Give the position of every malaria parasite.
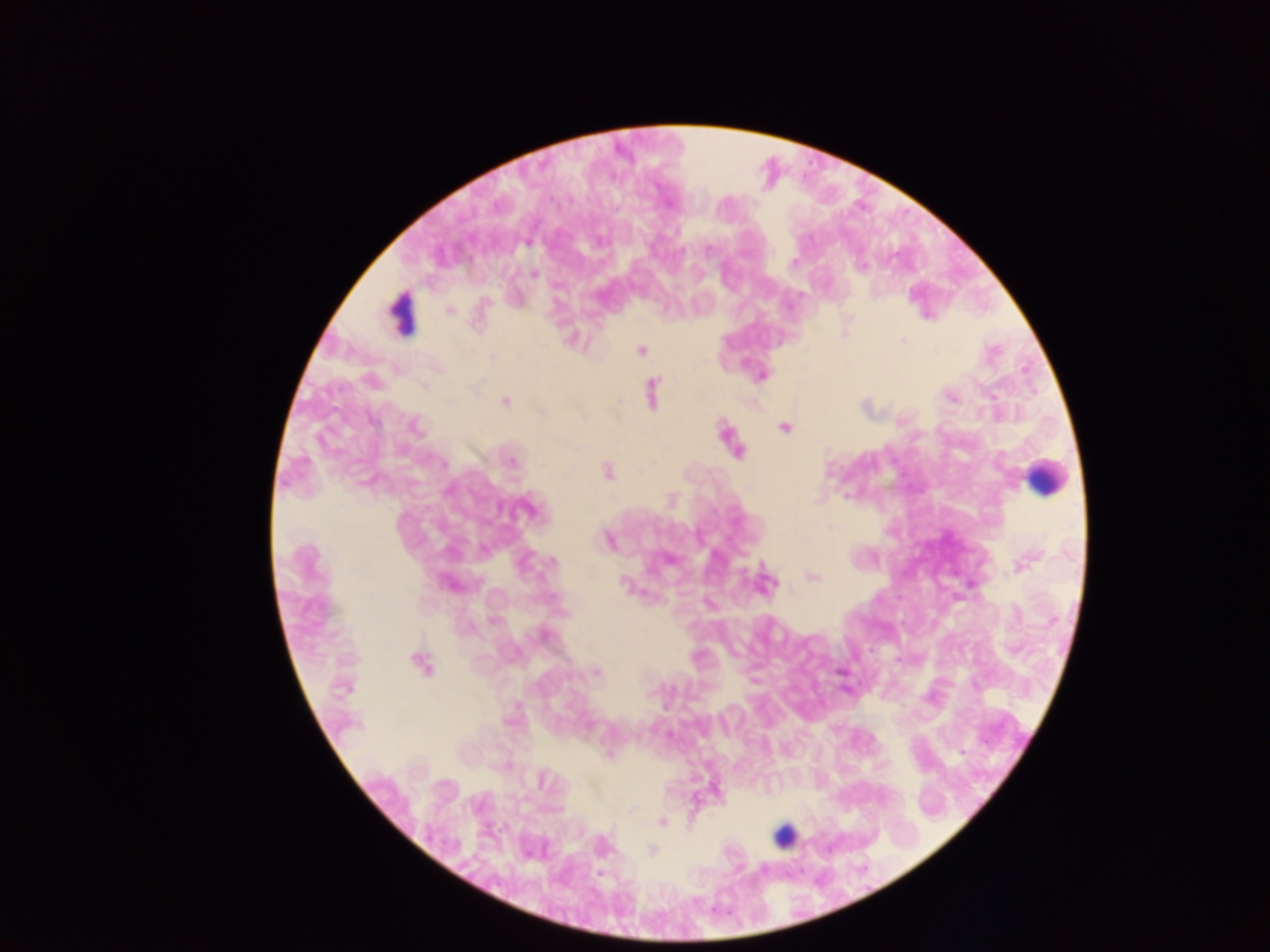
Approximate centers as x y in pixels.
Malaria parasites: 527 243; 709 252; 794 262; 861 266; 535 274; 449 310; 903 341; 641 350; 493 357; 761 375; 371 381; 652 393; 951 397; 506 401; 620 401; 542 412; 373 421; 415 427; 784 427; 736 450; 512 462; 444 463; 608 471; 526 509; 609 541; 553 561; 1023 564; 813 577; 767 581; 448 584; 624 584; 493 621; 544 634; 420 664; 596 673; 962 753; 609 754; 542 780; 663 823; 652 849.

Summary:
  - Leukocyte locations (subset; some below the resolvable size): 402 311; 1044 477; 784 836
  - Preparation: thick blood film
  - Capture: mobile-phone photograph through a microscope
  - Field of view: single
  - Image size: 1270×952 pixels
  - Country: Ghana